Assess this cell for malaria.
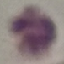
Uninfected.

Summary:
  - Stain: Giemsa
  - Image type: cell patch, automatically extracted from a larger field of view and resized to 64 × 64 pixels
  - Preparation: thin blood smear
  - Capture: smartphone through the microscope eyepiece